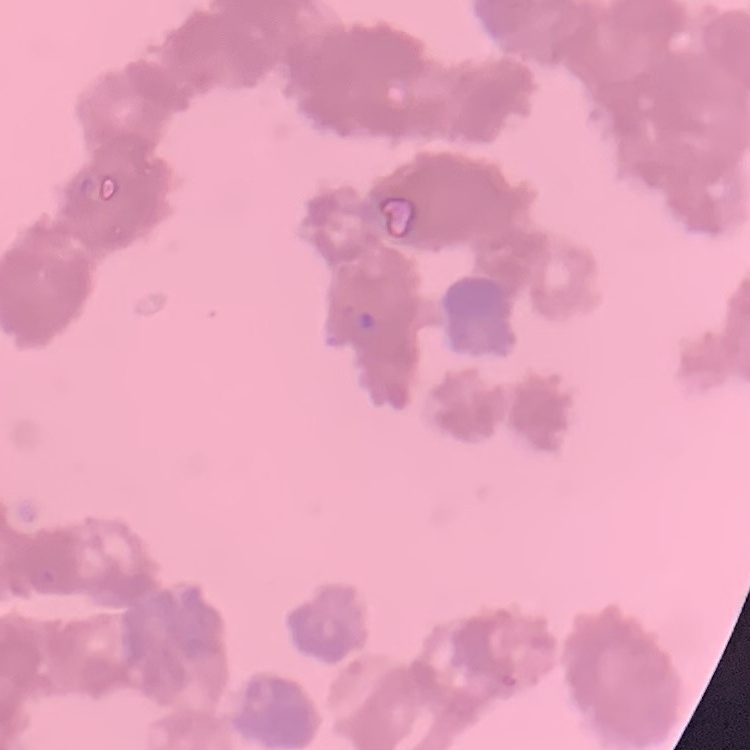
{
  "erythrocyte_morphology": "rouleaux formation",
  "stain": "Field's or Giemsa",
  "preparation": "thin blood film",
  "image_type": "one tile cut from a larger photomicrograph"
}